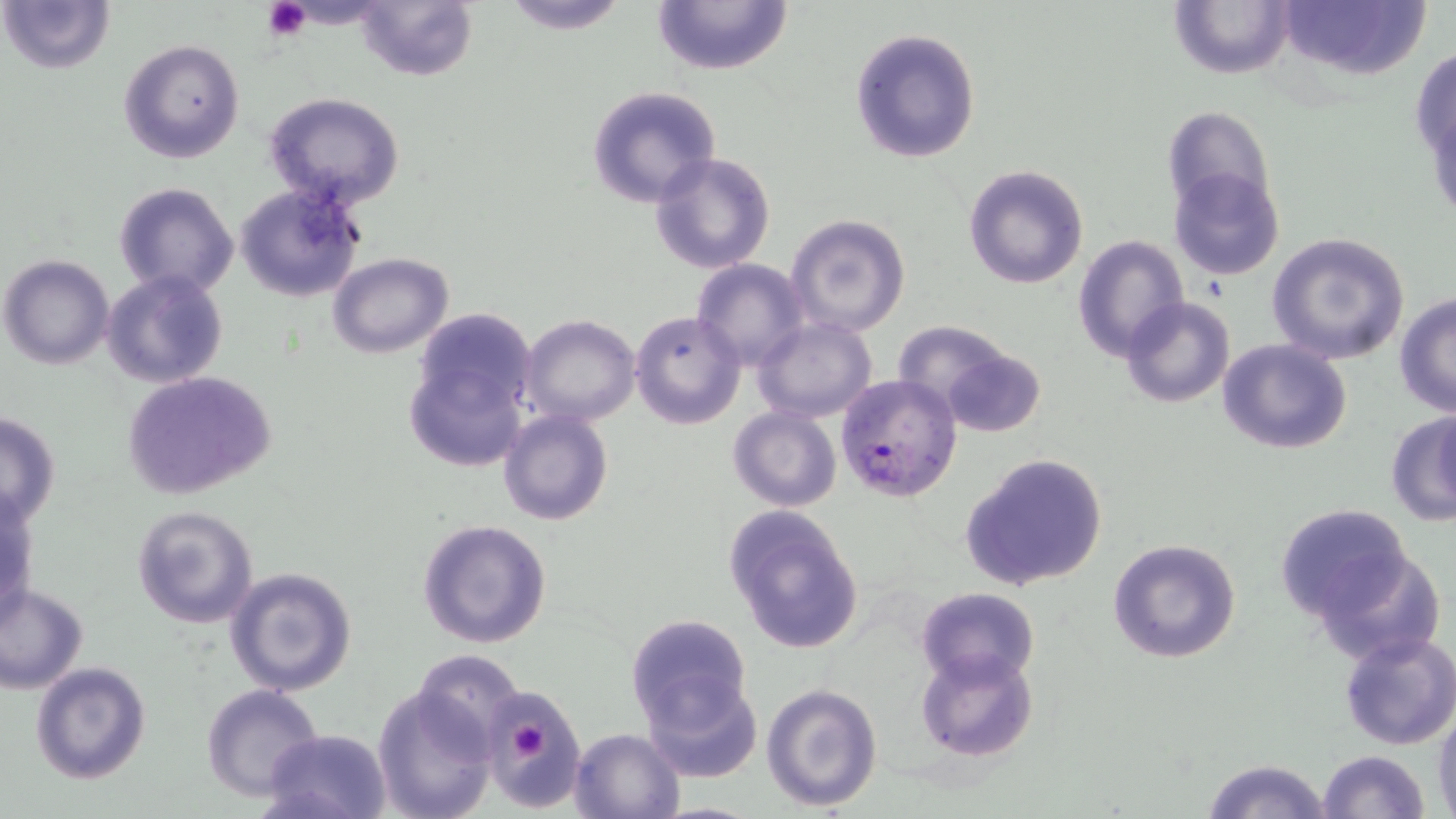
Summary:
  - Coordinate format: approximate bounding boxes as (x1, y1, x2, y2) in pixels
  - Plasmodium falciparum-infected red blood cell locations: (835, 374, 961, 502)
  - Platelet locations: (263, 0, 311, 40), (516, 725, 551, 760)
  - Uninfected red blood cell locations: (2, 0, 116, 74), (500, 0, 632, 34), (651, 0, 793, 76), (354, 1, 478, 83), (1169, 1, 1294, 80), (1277, 1, 1428, 80), (849, 26, 982, 165), (117, 38, 246, 164), (1410, 43, 1456, 183), (586, 85, 722, 209), (264, 91, 406, 211), (1161, 105, 1275, 219), (648, 152, 776, 275), (963, 164, 1090, 289), (1169, 167, 1286, 281), (112, 181, 241, 301), (233, 183, 366, 302), (787, 213, 910, 336), (1267, 232, 1410, 364), (1072, 235, 1188, 360), (330, 253, 453, 358), (2, 254, 115, 370), (690, 258, 811, 371), (104, 271, 227, 388), (1393, 292, 1456, 417), (1119, 296, 1235, 407), (629, 310, 745, 429), (518, 314, 641, 425), (404, 315, 536, 474), (752, 317, 877, 423), (894, 322, 1045, 435), (1217, 339, 1353, 456), (122, 370, 275, 501), (727, 406, 843, 512), (1385, 409, 1456, 527), (498, 410, 614, 527), (0, 413, 61, 529), (960, 453, 1108, 592), (1, 486, 38, 624), (131, 503, 258, 629), (1274, 504, 1417, 625), (723, 507, 866, 654), (416, 519, 552, 649), (1106, 537, 1242, 665), (1310, 545, 1447, 667), (225, 565, 357, 697), (0, 583, 89, 693), (913, 586, 1041, 689), (624, 613, 754, 734), (1337, 632, 1456, 750), (916, 648, 1039, 761), (412, 649, 522, 754), (30, 662, 151, 784), (642, 671, 762, 783), (761, 681, 885, 815), (202, 684, 326, 802), (372, 685, 498, 819), (483, 685, 587, 808), (1432, 706, 1456, 819), (569, 727, 687, 818), (265, 730, 391, 819), (1317, 748, 1432, 819), (1199, 758, 1336, 818)
  - Slide-level diagnosis: Plasmodium falciparum
  - Field of view: one of a larger specimen
  - Preparation: thin blood smear
  - Image size: 1456×819 pixels
  - Modality: light microscopy
  - Stain: May-Grünwald-Giemsa
  - Magnification: 1000x